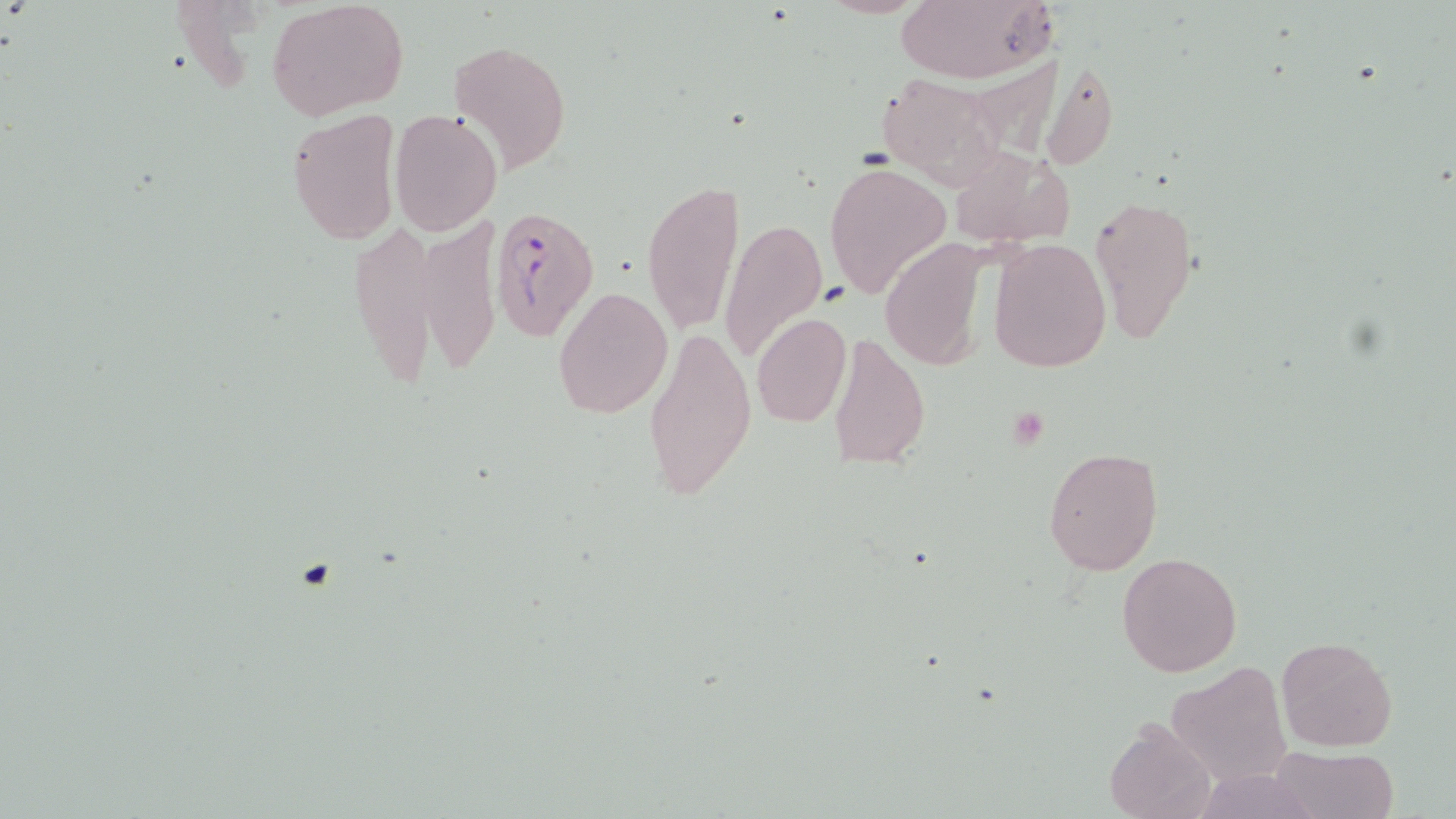
Summary:
  - Coordinate format: approximate bounding boxes as named x1/y1/x2/y2 corners in pixels
  - Platelet locations: (x1=296, y1=558, x2=336, y2=593)
  - Plasmodium falciparum-infected red blood cell locations: (x1=491, y1=204, x2=597, y2=341)
  - Uninfected red blood cell locations: (x1=266, y1=0, x2=408, y2=118), (x1=893, y1=0, x2=1053, y2=83), (x1=449, y1=38, x2=573, y2=179), (x1=1038, y1=59, x2=1119, y2=172), (x1=875, y1=70, x2=1009, y2=186), (x1=286, y1=109, x2=400, y2=248), (x1=389, y1=109, x2=502, y2=235), (x1=946, y1=146, x2=1074, y2=247), (x1=824, y1=161, x2=950, y2=299), (x1=640, y1=178, x2=744, y2=336), (x1=1089, y1=194, x2=1200, y2=343), (x1=349, y1=216, x2=440, y2=394), (x1=416, y1=216, x2=501, y2=380), (x1=718, y1=218, x2=828, y2=364), (x1=987, y1=237, x2=1112, y2=374), (x1=878, y1=238, x2=997, y2=371), (x1=553, y1=286, x2=673, y2=417), (x1=751, y1=312, x2=852, y2=428), (x1=644, y1=322, x2=757, y2=508), (x1=828, y1=329, x2=931, y2=472), (x1=1043, y1=446, x2=1163, y2=574), (x1=1116, y1=552, x2=1243, y2=679), (x1=1276, y1=636, x2=1398, y2=752), (x1=1167, y1=661, x2=1292, y2=785), (x1=1104, y1=720, x2=1215, y2=819), (x1=1270, y1=745, x2=1398, y2=819), (x1=1194, y1=766, x2=1322, y2=819)
  - Slide-level diagnosis: Plasmodium falciparum
  - Image size: 1456×819 pixels
  - Field of view: single
  - Stain: May-Grünwald-Giemsa
  - Modality: light microscopy
  - Magnification: 1000x
  - Preparation: thin blood smear